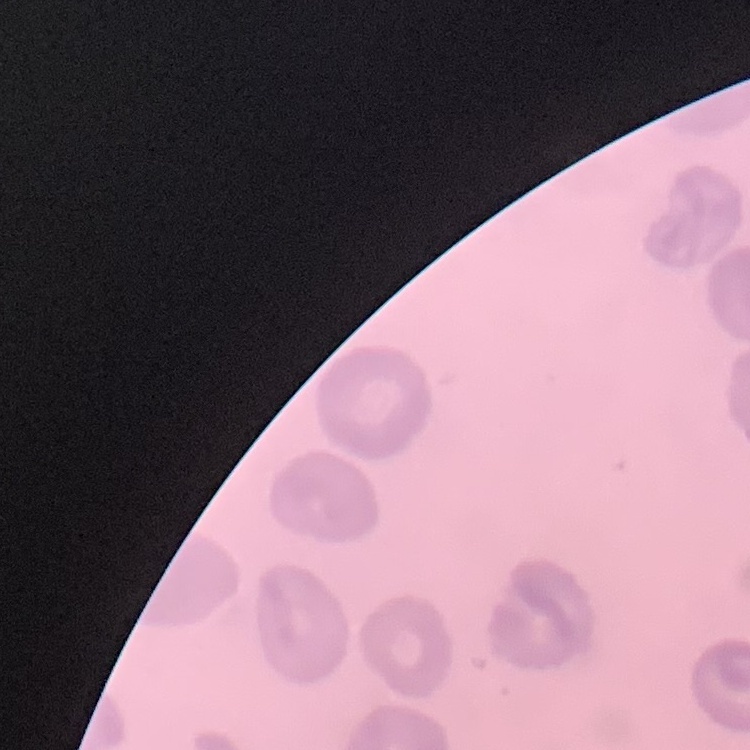

erythrocyte morphology = no rouleaux formation
preparation = thin peripheral smear
stain = Field's or Giemsa
image type = square crop of a larger photomicrograph